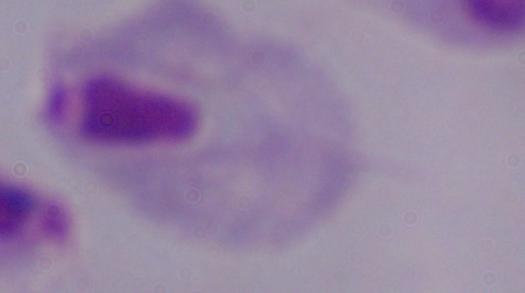

Summary:
  - Modality: photomicrograph
  - Identification: trichomonad
  - Magnification: 1000x